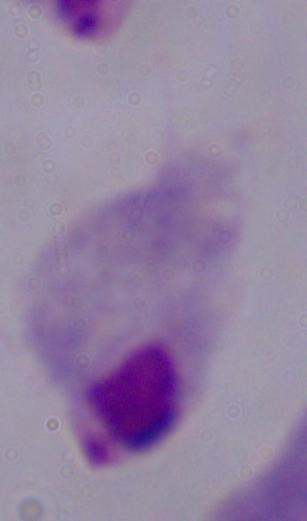

modality = micrograph
magnification = 1000x
identification = trichomonad